Assess this cell for malaria.
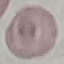

Uninfected.

Summary:
  - Capture: smartphone through the microscope eyepiece
  - Image type: automatically extracted cell patch, resized to 64 × 64 pixels
  - Preparation: thin blood film
  - Stain: Giemsa